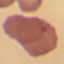
Malaria status: uninfected. Giemsa stain. Thin blood film. Automatically extracted cell patch, resized to 64 × 64 pixels. Photographed with a smartphone camera at the microscope eyepiece.